Locate and identify every blood parasite.
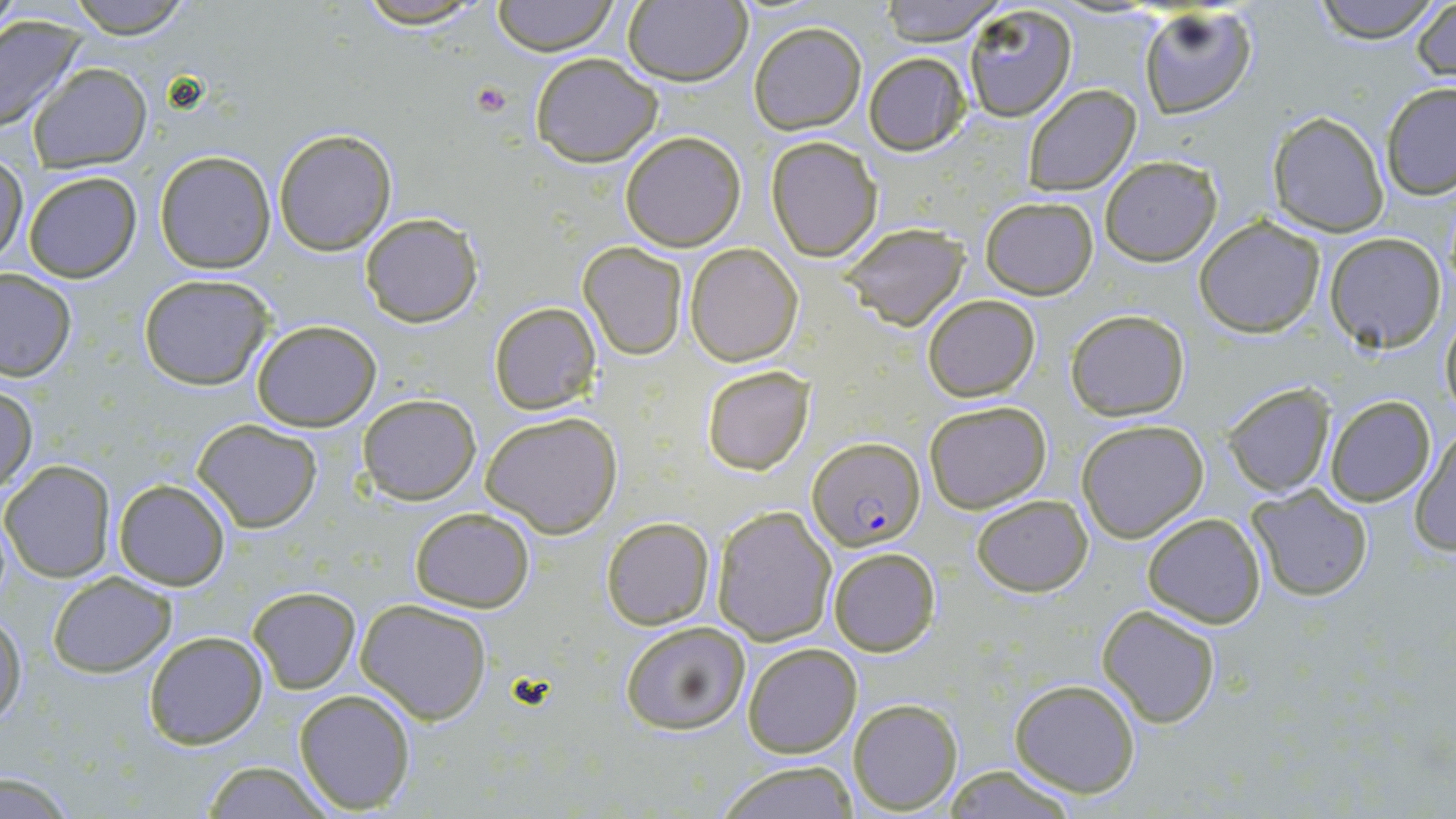

Approximate bounding boxes as (x1, y1, x2, y2) in pixels.
Plasmodium falciparum-infected red blood cells: (805, 436, 924, 549).
No Plasmodium ovale, Plasmodium malariae, Plasmodium vivax, Babesia divergens, or Trypanosoma brucei observed.

Uninfected red blood cell locations: (64, 0, 197, 39), (349, 0, 493, 27), (491, 0, 617, 55), (623, 0, 750, 85), (878, 0, 1003, 44), (1311, 0, 1441, 43), (1412, 2, 1454, 83), (961, 3, 1078, 121), (1139, 7, 1255, 119), (0, 14, 88, 135), (748, 21, 867, 134), (528, 53, 663, 167), (863, 53, 971, 155), (27, 62, 152, 171), (1382, 83, 1456, 200), (1024, 84, 1141, 196), (1267, 111, 1390, 237), (273, 127, 397, 254), (619, 131, 746, 251), (766, 135, 882, 261), (154, 150, 276, 273), (1099, 156, 1221, 266), (0, 158, 27, 268), (20, 171, 142, 283), (980, 196, 1098, 299), (359, 213, 484, 328), (1194, 217, 1326, 336), (838, 221, 970, 330), (1326, 232, 1446, 353), (578, 241, 687, 360), (686, 243, 802, 366), (0, 268, 77, 381), (137, 275, 274, 392), (921, 294, 1041, 403), (489, 302, 601, 414), (1065, 310, 1190, 422), (1439, 310, 1455, 415), (252, 319, 381, 431), (700, 365, 815, 475), (1223, 382, 1336, 497), (1, 384, 38, 493), (357, 392, 481, 504), (1325, 395, 1436, 507), (923, 400, 1053, 514), (480, 411, 624, 538), (1075, 418, 1210, 542), (193, 421, 322, 533), (1410, 426, 1456, 556), (2, 460, 115, 582), (113, 478, 230, 589), (1246, 485, 1373, 602), (971, 494, 1094, 596), (712, 505, 836, 645), (409, 507, 537, 612), (1142, 511, 1266, 628), (601, 516, 715, 630), (827, 545, 940, 658), (46, 571, 175, 677), (248, 586, 360, 693), (356, 599, 493, 724), (1096, 603, 1222, 730), (0, 611, 28, 728), (620, 619, 752, 735), (142, 630, 269, 749), (742, 642, 862, 757), (1009, 677, 1142, 799), (293, 688, 415, 814), (847, 696, 962, 814), (710, 760, 863, 819), (199, 762, 337, 818), (938, 765, 1086, 818), (0, 775, 79, 816). Platelet locations: (471, 80, 512, 115). Slide-level diagnosis: Plasmodium falciparum. Optical microscopy. Thin blood smear. Image is 1456×819 pixels. Captured at 1000x magnification. May-Grünwald-Giemsa stain. One field of a larger specimen.